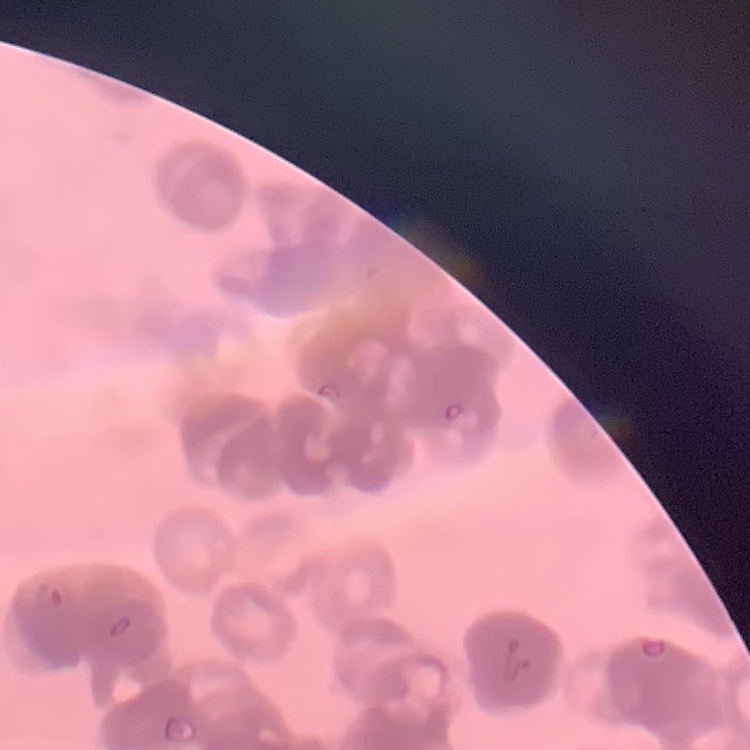
Summary:
  - Erythrocyte morphology: rouleaux formation
  - Image type: one tile cut from a larger photomicrograph
  - Preparation: thin blood film
  - Stain: Field's or Giemsa